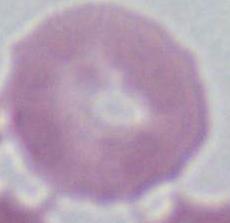

{
  "identification": "red blood cell",
  "modality": "photomicrograph",
  "magnification": "1000x"
}